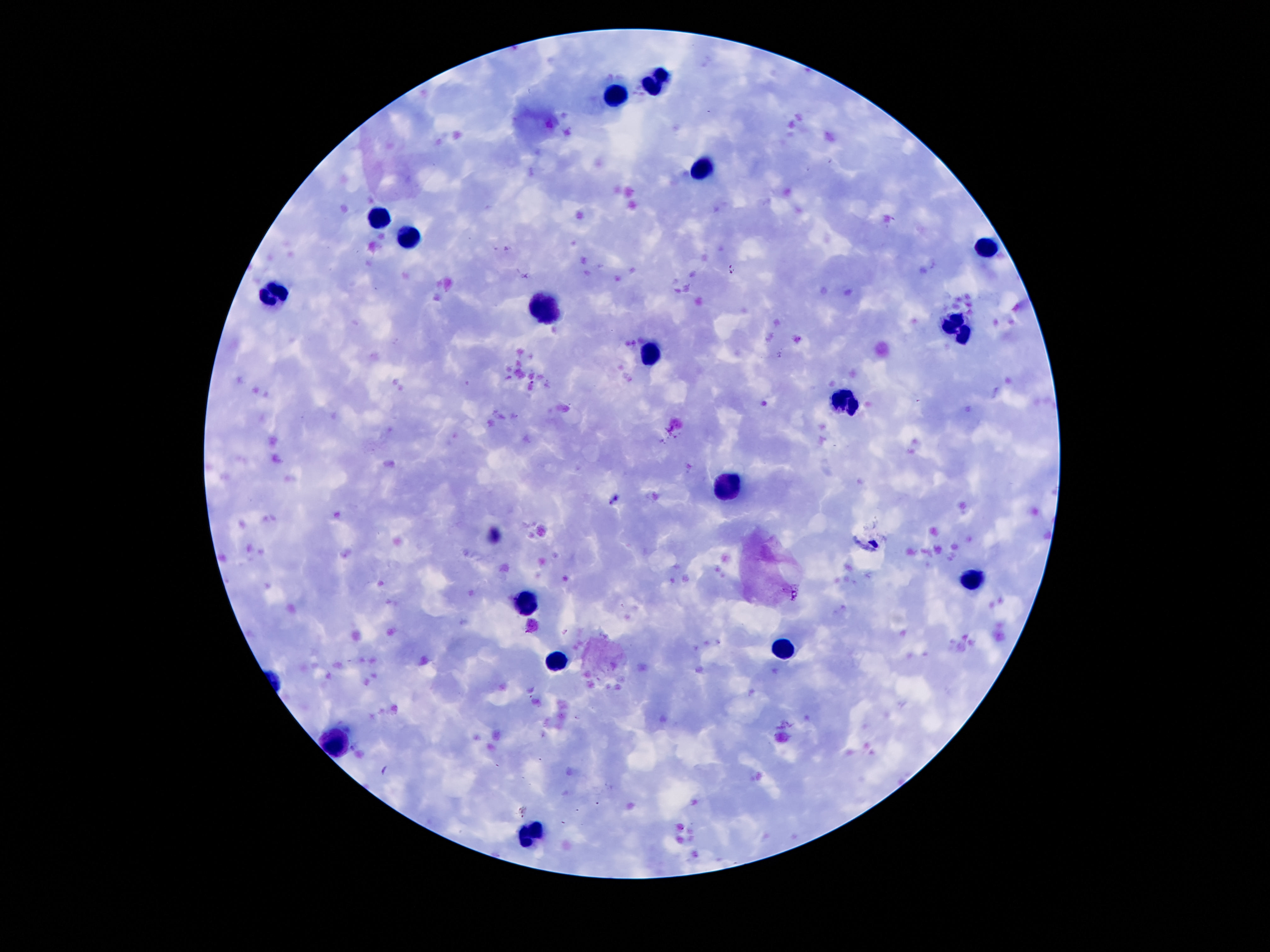
Approximate object centers, in pixels from the top-left corner. Leukocyte locations: (x=657, y=81), (x=614, y=95), (x=700, y=171), (x=382, y=216), (x=407, y=236), (x=983, y=250), (x=274, y=291), (x=546, y=312), (x=960, y=326), (x=651, y=357), (x=843, y=406), (x=727, y=484), (x=973, y=578), (x=526, y=601), (x=788, y=650), (x=555, y=662), (x=337, y=742), (x=530, y=830). 100x magnification. Thick peripheral-blood smear. Image is 1270×952 pixels. Patient malaria status: negative. One field from this slide. Giemsa-stained preparation. Photographed through the microscope eyepiece with a smartphone camera.